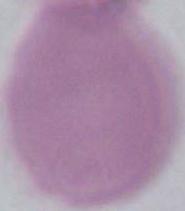

modality = photomicrograph
identification = red blood cell
magnification = 1000x